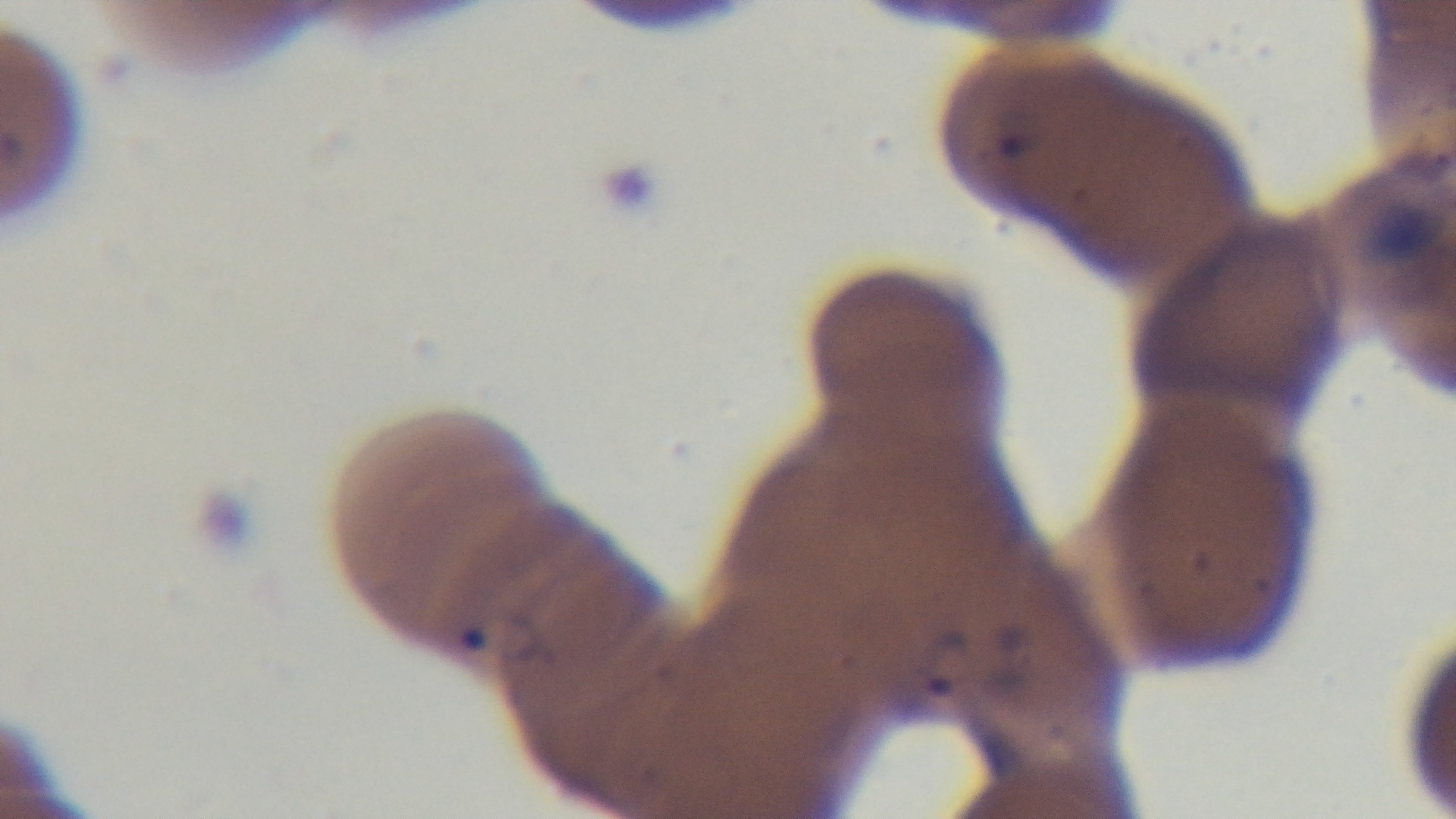

Light microscopy. 100x oil-immersion objective. Preparation: thin smear. Malaria status: infected. Mounted 4K digital camera. Giemsa-stained. Single field of view.